Name the blood parasite species.
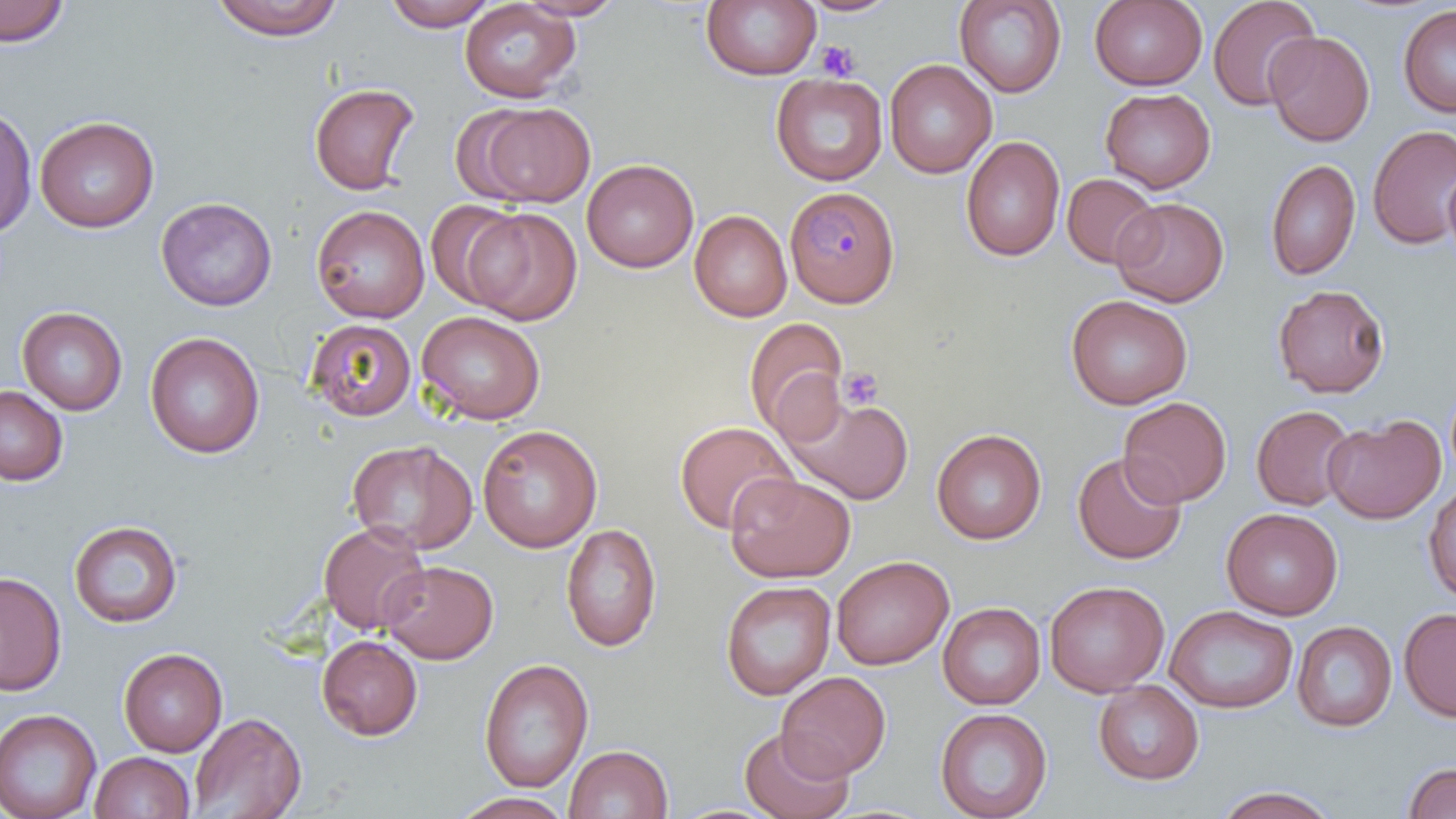
Plasmodium malariae.

Approximate bounding boxes as (x1, y1, x2, y2) in pixels. Platelet locations: (815, 41, 860, 82), (838, 366, 884, 411). Uninfected red blood cell locations: (0, 0, 69, 46), (210, 0, 345, 40), (381, 0, 497, 30), (515, 0, 627, 20), (1089, 0, 1208, 91), (1207, 0, 1319, 111), (459, 1, 580, 103), (701, 1, 821, 81), (797, 1, 903, 17), (954, 1, 1067, 97), (1397, 6, 1456, 118), (1264, 30, 1375, 147), (885, 59, 997, 179), (771, 73, 888, 186), (309, 83, 420, 195), (1100, 87, 1215, 193), (473, 103, 595, 207), (0, 105, 37, 238), (35, 116, 159, 233), (1367, 125, 1456, 249), (960, 136, 1066, 262), (1264, 158, 1360, 282), (582, 159, 699, 273), (1443, 163, 1456, 270), (1061, 173, 1161, 268), (156, 196, 277, 311), (1112, 197, 1229, 307), (425, 200, 526, 309), (311, 205, 430, 323), (466, 208, 582, 325), (690, 210, 792, 321), (1272, 284, 1391, 398), (1066, 294, 1193, 410), (17, 306, 127, 414), (417, 310, 545, 425), (744, 317, 848, 440), (304, 318, 416, 421), (145, 332, 265, 458), (0, 385, 68, 485), (782, 393, 914, 505), (1118, 397, 1231, 507), (1251, 405, 1356, 511), (1322, 414, 1446, 524), (674, 421, 797, 534), (477, 424, 602, 552), (931, 428, 1046, 545), (347, 439, 478, 555), (1072, 451, 1186, 564), (726, 474, 855, 583), (1423, 482, 1456, 603), (1221, 507, 1343, 620), (68, 520, 183, 628), (318, 521, 431, 634), (560, 523, 662, 652), (832, 555, 954, 669), (380, 560, 498, 664), (0, 571, 66, 695), (720, 580, 836, 700), (1044, 580, 1169, 697), (937, 602, 1045, 710), (1165, 605, 1298, 714), (1398, 607, 1456, 722), (1292, 621, 1397, 732), (317, 635, 423, 741), (118, 648, 227, 757), (478, 658, 593, 793), (776, 671, 891, 780), (1093, 680, 1204, 785), (934, 707, 1052, 819), (0, 708, 101, 819), (188, 711, 307, 818), (740, 727, 853, 819), (564, 744, 673, 819), (90, 751, 195, 819), (1402, 762, 1456, 819), (1213, 785, 1339, 819), (451, 792, 575, 819). Plasmodium malariae-infected red blood cell locations: (786, 186, 900, 308). Optical microscopy. Thin blood film. Image is 1456×819 pixels. Single field of view. May-Grünwald-Giemsa stain. Captured at 1000x magnification.